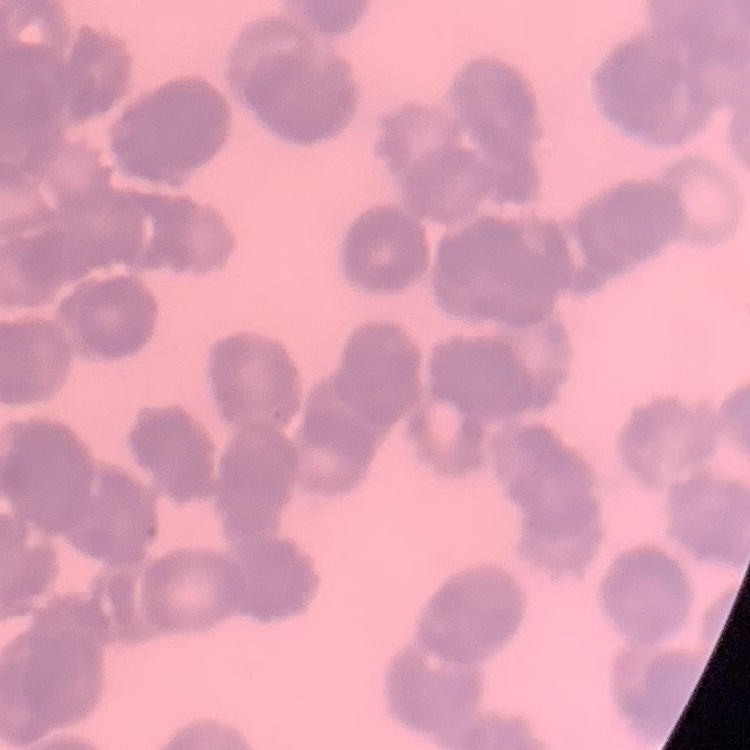
The red blood cells show rouleaux formation. Field's or Giemsa stain. Square crop of a larger photomicrograph. Thin peripheral smear.